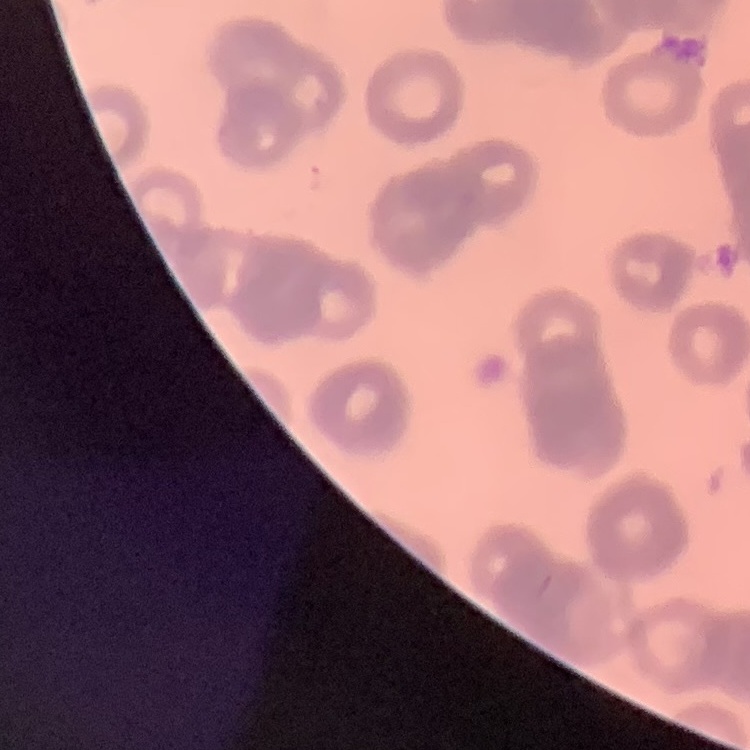

The red blood cells show rouleaux formation. Thin peripheral smear. Stained with either Field's or Giemsa. Square crop of a larger photomicrograph.